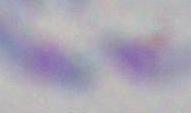

Micrograph. Captured at 1000x magnification. Toxoplasma gondii is shown.